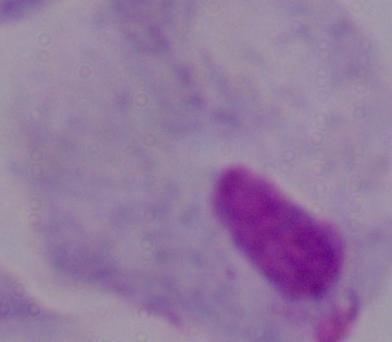
Photomicrograph. Captured at 1000x magnification. A trichomonad is seen.